Locate and identify every blood parasite.
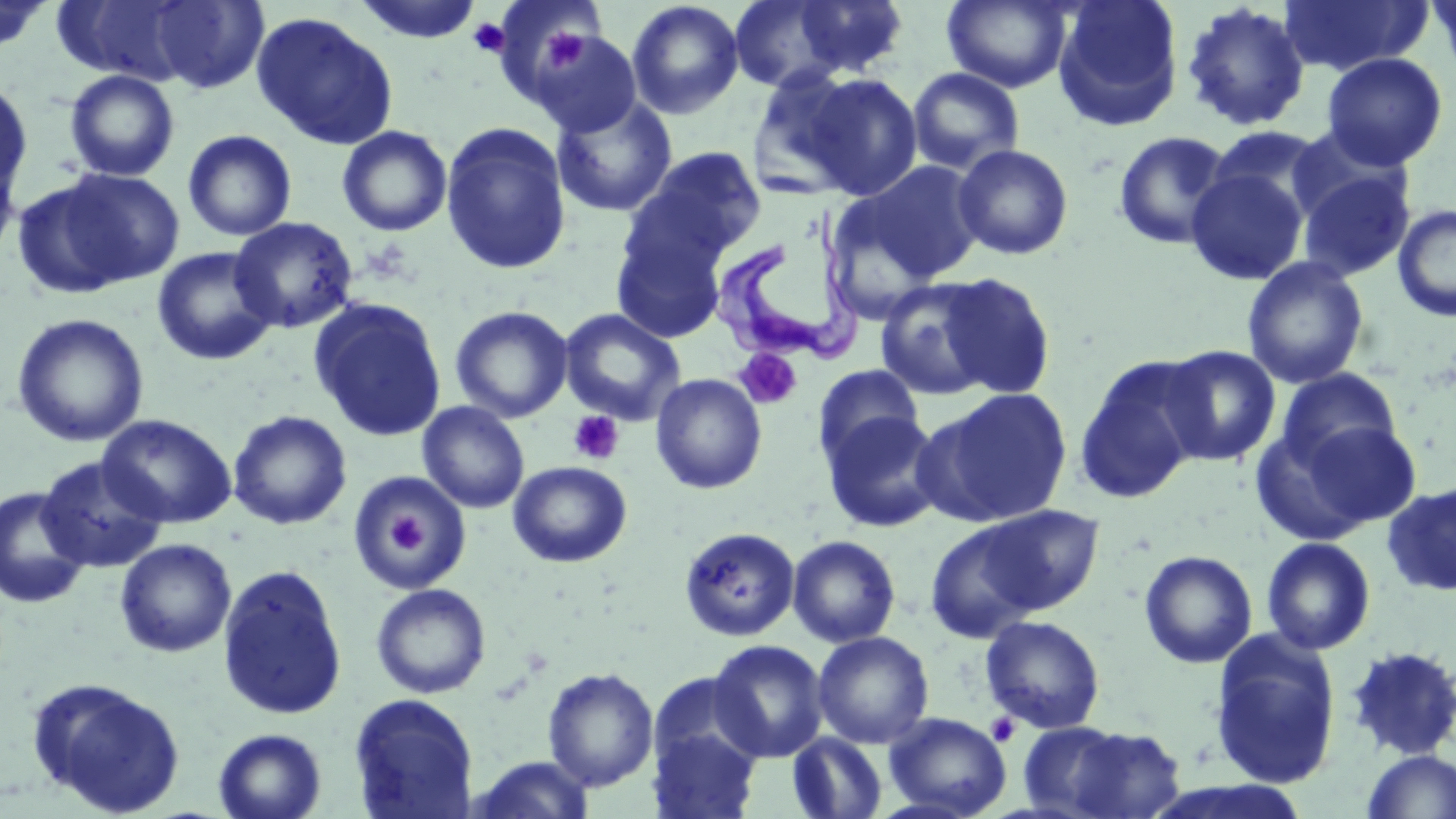

Approximate bounding boxes as named x1/y1/x2/y2 corners in pixels.
Trypanosoma brucei: (x1=710, y1=203, x2=862, y2=366).
No Plasmodium falciparum, Plasmodium ovale, Plasmodium malariae, Plasmodium vivax, or Babesia divergens observed.

Uninfected red blood cell locations: (x1=354, y1=0, x2=483, y2=44), (x1=728, y1=0, x2=852, y2=92), (x1=789, y1=0, x2=910, y2=78), (x1=942, y1=0, x2=1073, y2=92), (x1=1052, y1=0, x2=1184, y2=131), (x1=1278, y1=0, x2=1430, y2=76), (x1=1425, y1=0, x2=1456, y2=86), (x1=0, y1=1, x2=56, y2=55), (x1=626, y1=1, x2=744, y2=119), (x1=143, y1=2, x2=270, y2=92), (x1=1180, y1=2, x2=1312, y2=133), (x1=501, y1=4, x2=609, y2=96), (x1=250, y1=11, x2=398, y2=149), (x1=529, y1=29, x2=641, y2=136), (x1=1322, y1=52, x2=1448, y2=170), (x1=907, y1=67, x2=1025, y2=176), (x1=64, y1=69, x2=180, y2=181), (x1=747, y1=69, x2=868, y2=197), (x1=801, y1=72, x2=924, y2=200), (x1=0, y1=77, x2=34, y2=201), (x1=551, y1=95, x2=678, y2=218), (x1=439, y1=122, x2=572, y2=275), (x1=336, y1=125, x2=453, y2=236), (x1=1205, y1=126, x2=1332, y2=223), (x1=183, y1=130, x2=297, y2=241), (x1=1113, y1=130, x2=1234, y2=251), (x1=0, y1=141, x2=22, y2=266), (x1=952, y1=144, x2=1074, y2=260), (x1=630, y1=146, x2=767, y2=263), (x1=855, y1=161, x2=987, y2=284), (x1=1186, y1=164, x2=1309, y2=285), (x1=31, y1=167, x2=185, y2=292), (x1=1296, y1=167, x2=1415, y2=281), (x1=1392, y1=204, x2=1456, y2=322), (x1=229, y1=217, x2=358, y2=334), (x1=611, y1=219, x2=729, y2=344), (x1=152, y1=247, x2=279, y2=366), (x1=1243, y1=257, x2=1369, y2=389), (x1=932, y1=272, x2=1056, y2=399), (x1=875, y1=277, x2=1003, y2=400), (x1=309, y1=298, x2=446, y2=441), (x1=450, y1=305, x2=573, y2=423), (x1=560, y1=309, x2=686, y2=426), (x1=11, y1=313, x2=149, y2=447), (x1=1160, y1=345, x2=1281, y2=466), (x1=1074, y1=357, x2=1207, y2=503), (x1=813, y1=364, x2=923, y2=468), (x1=1275, y1=369, x2=1400, y2=470), (x1=649, y1=373, x2=767, y2=494), (x1=920, y1=388, x2=1073, y2=527), (x1=418, y1=401, x2=529, y2=513), (x1=228, y1=410, x2=352, y2=530), (x1=820, y1=410, x2=946, y2=533), (x1=97, y1=414, x2=237, y2=528), (x1=1279, y1=418, x2=1424, y2=534), (x1=36, y1=456, x2=168, y2=574), (x1=508, y1=460, x2=632, y2=567), (x1=347, y1=471, x2=473, y2=597), (x1=1382, y1=482, x2=1456, y2=597), (x1=0, y1=486, x2=92, y2=609), (x1=974, y1=505, x2=1104, y2=615), (x1=924, y1=522, x2=1045, y2=643), (x1=679, y1=527, x2=800, y2=642), (x1=787, y1=535, x2=901, y2=648), (x1=1260, y1=537, x2=1376, y2=655), (x1=114, y1=538, x2=237, y2=658), (x1=1138, y1=550, x2=1258, y2=668), (x1=216, y1=564, x2=348, y2=720), (x1=371, y1=583, x2=491, y2=699), (x1=980, y1=615, x2=1105, y2=734), (x1=813, y1=630, x2=934, y2=749), (x1=1209, y1=632, x2=1342, y2=790), (x1=709, y1=639, x2=829, y2=762), (x1=1344, y1=645, x2=1456, y2=761), (x1=542, y1=667, x2=659, y2=791), (x1=646, y1=671, x2=764, y2=781), (x1=27, y1=677, x2=185, y2=817), (x1=348, y1=693, x2=479, y2=819), (x1=883, y1=711, x2=1011, y2=818), (x1=1024, y1=722, x2=1183, y2=818), (x1=647, y1=725, x2=762, y2=818), (x1=213, y1=728, x2=327, y2=819), (x1=787, y1=732, x2=888, y2=819), (x1=1360, y1=749, x2=1456, y2=819), (x1=466, y1=755, x2=597, y2=818). Platelet locations: (x1=469, y1=17, x2=510, y2=57), (x1=539, y1=26, x2=585, y2=72), (x1=734, y1=348, x2=803, y2=410), (x1=567, y1=410, x2=624, y2=465), (x1=383, y1=505, x2=433, y2=561), (x1=985, y1=713, x2=1021, y2=746). Slide-level diagnosis: Trypanosoma brucei. Optical microscopy. May-Grünwald-Giemsa stain. 1000x magnification. Single field of view. Thin blood smear. Image is 1456×819 pixels.